Describe the morphology of the red blood cells.
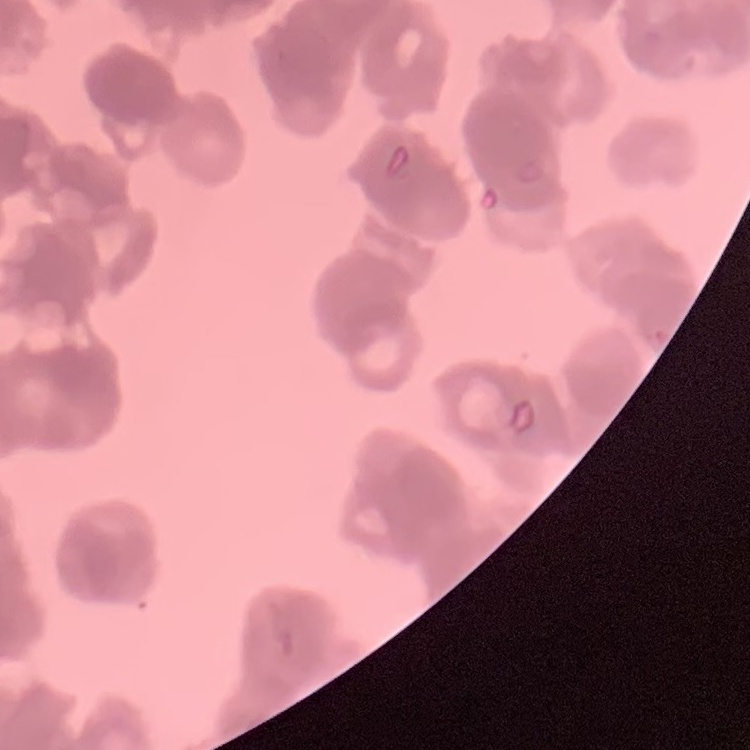

Rouleaux formation.

Summary:
  - Image type: square crop of a larger photomicrograph
  - Preparation: thin peripheral smear
  - Stain: Field's or Giemsa